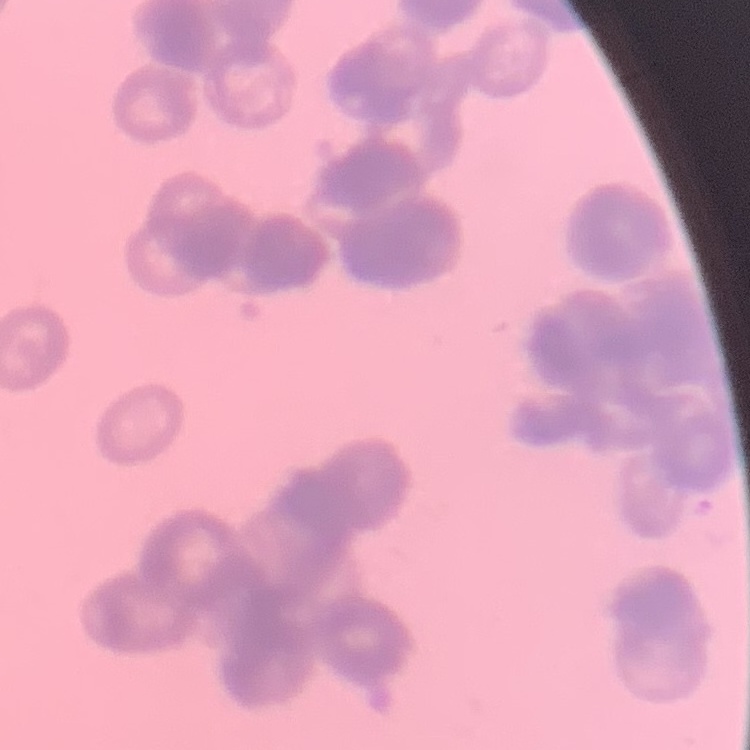

Summary:
  - Erythrocyte morphology: rouleaux formation
  - Image type: square crop of a larger photomicrograph
  - Stain: Field's or Giemsa
  - Preparation: thin blood film